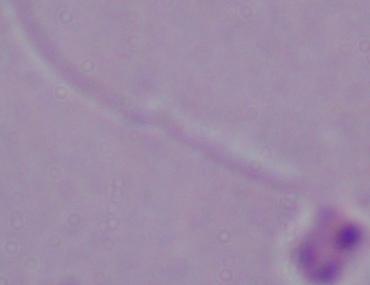 Photomicrograph. Captured at 1000x magnification. A Leishmania parasite is seen.